Outline each Trypanosoma brucei.
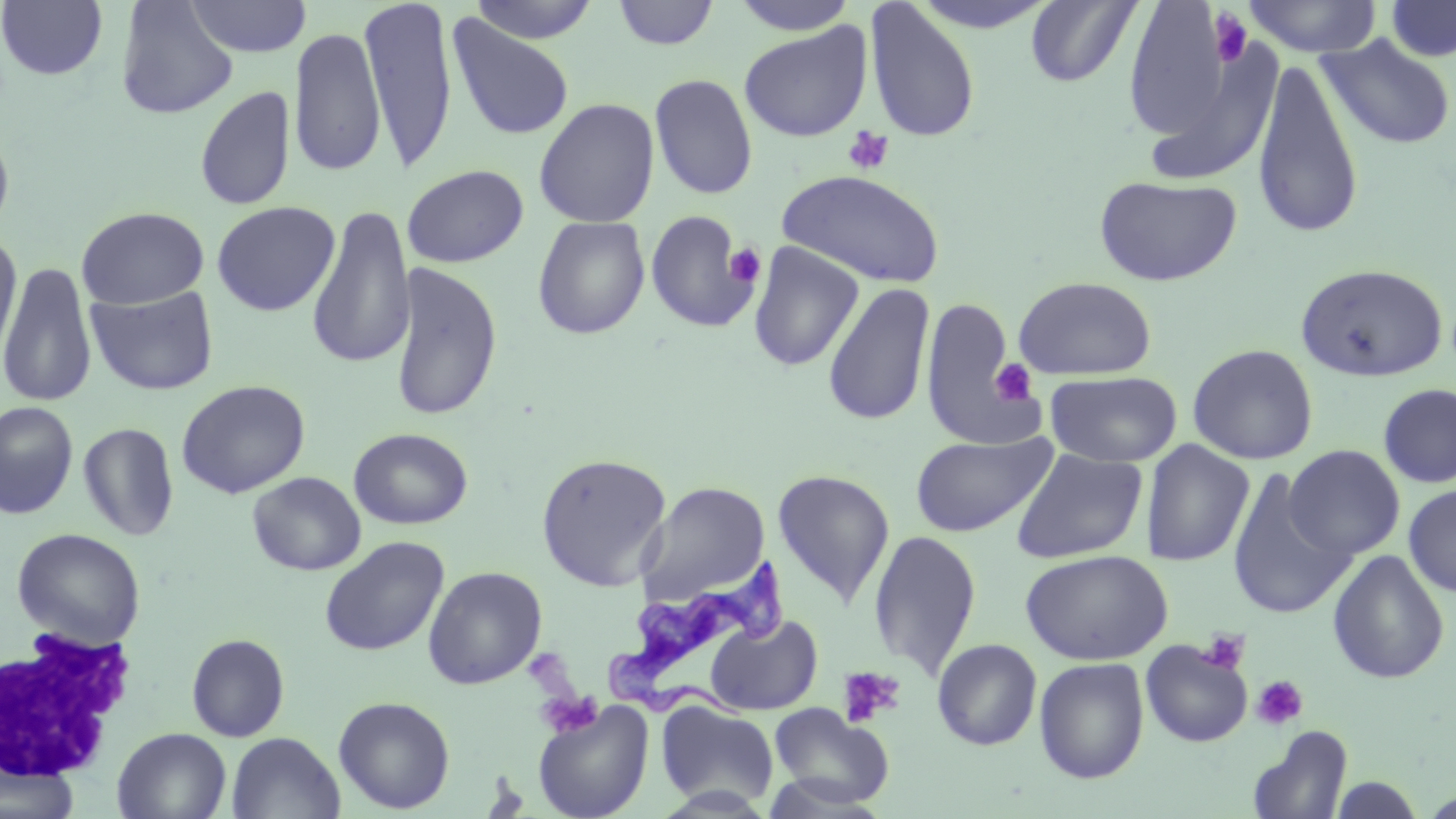

Approximate bounding boxes as (x1,y1)-(x2,y2) corner pairs in pixels.
Trypanosoma brucei: (603,556)-(787,709).

White blood cell locations: (0,625)-(139,784). Uninfected red blood cell locations: (184,0)-(311,58), (359,0)-(459,174), (469,0)-(600,44), (727,0)-(862,35), (908,0)-(1060,34), (1241,0)-(1383,57), (1385,0)-(1456,62), (0,1)-(108,81), (114,1)-(239,119), (612,1)-(719,50), (1024,1)-(1141,87), (864,2)-(981,143), (1121,2)-(1231,141), (447,14)-(576,142), (739,22)-(871,142), (289,26)-(385,177), (1318,34)-(1455,151), (1252,57)-(1363,242), (649,73)-(758,200), (195,85)-(295,211), (533,97)-(660,228), (0,119)-(16,242), (401,164)-(529,268), (777,169)-(946,289), (1094,174)-(1243,286), (211,201)-(339,316), (306,204)-(414,371), (76,206)-(209,309), (645,211)-(758,334), (532,216)-(650,340), (1,235)-(24,368), (747,242)-(864,372), (0,261)-(97,408), (389,261)-(502,423), (1295,262)-(1448,382), (1013,276)-(1157,380), (822,282)-(935,427), (85,284)-(220,396), (921,295)-(1036,451), (1187,343)-(1319,465), (1044,370)-(1182,468), (176,379)-(310,498), (1378,383)-(1456,488), (0,401)-(78,519), (78,422)-(179,541), (349,427)-(473,530), (910,431)-(1056,538), (1140,439)-(1255,567), (1284,445)-(1405,560), (1010,447)-(1148,564), (535,453)-(671,591), (1226,468)-(1355,621), (771,469)-(895,608), (247,472)-(365,576), (637,481)-(770,605), (1403,483)-(1456,596), (12,528)-(146,649), (867,529)-(982,680), (319,536)-(450,656), (1019,549)-(1172,665), (1327,549)-(1450,685), (423,567)-(547,690), (704,615)-(823,715), (186,634)-(290,742), (932,638)-(1042,751), (1140,639)-(1253,748), (1034,657)-(1149,784), (333,696)-(455,814), (533,700)-(654,819), (655,701)-(779,810), (768,704)-(894,811), (1247,725)-(1353,819), (112,728)-(231,818), (226,732)-(344,818), (1,758)-(79,819), (1328,774)-(1427,817). Platelet locations: (1208,9)-(1253,66), (843,127)-(894,175), (724,243)-(766,288), (990,358)-(1039,405), (1199,629)-(1251,675), (836,666)-(906,729), (1251,675)-(1309,731), (535,690)-(604,739). Slide-level diagnosis: Trypanosoma brucei. Thin blood smear. 1000x magnification. One field of a larger specimen. Optical microscopy. Image is 1456×819 pixels. May-Grünwald-Giemsa stain.